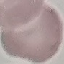
Summary:
  - Malaria status: uninfected
  - Image type: automatically extracted cell patch, resized to 64 × 64 pixels
  - Stain: Giemsa
  - Preparation: thin smear
  - Capture: smartphone camera at the microscope eyepiece